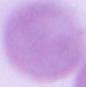
Summary:
  - Identification: red blood cell
  - Magnification: 1000x
  - Modality: micrograph